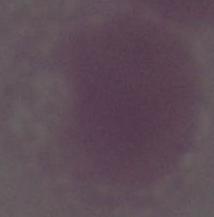
Summary:
  - Magnification: 1000x
  - Identification: red blood cell
  - Modality: photomicrograph